Identify the cell.
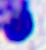
A leukocyte.

Summary:
  - Magnification: 400x
  - Modality: micrograph